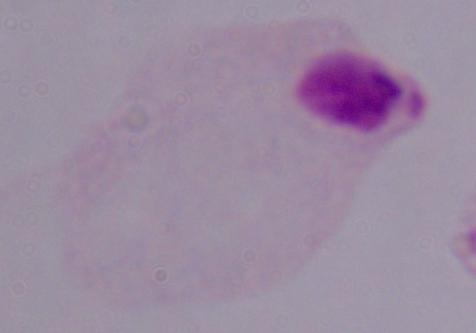
{
  "modality": "photomicrograph",
  "magnification": "1000x",
  "identification": "trichomonad"
}